Outline platelets.
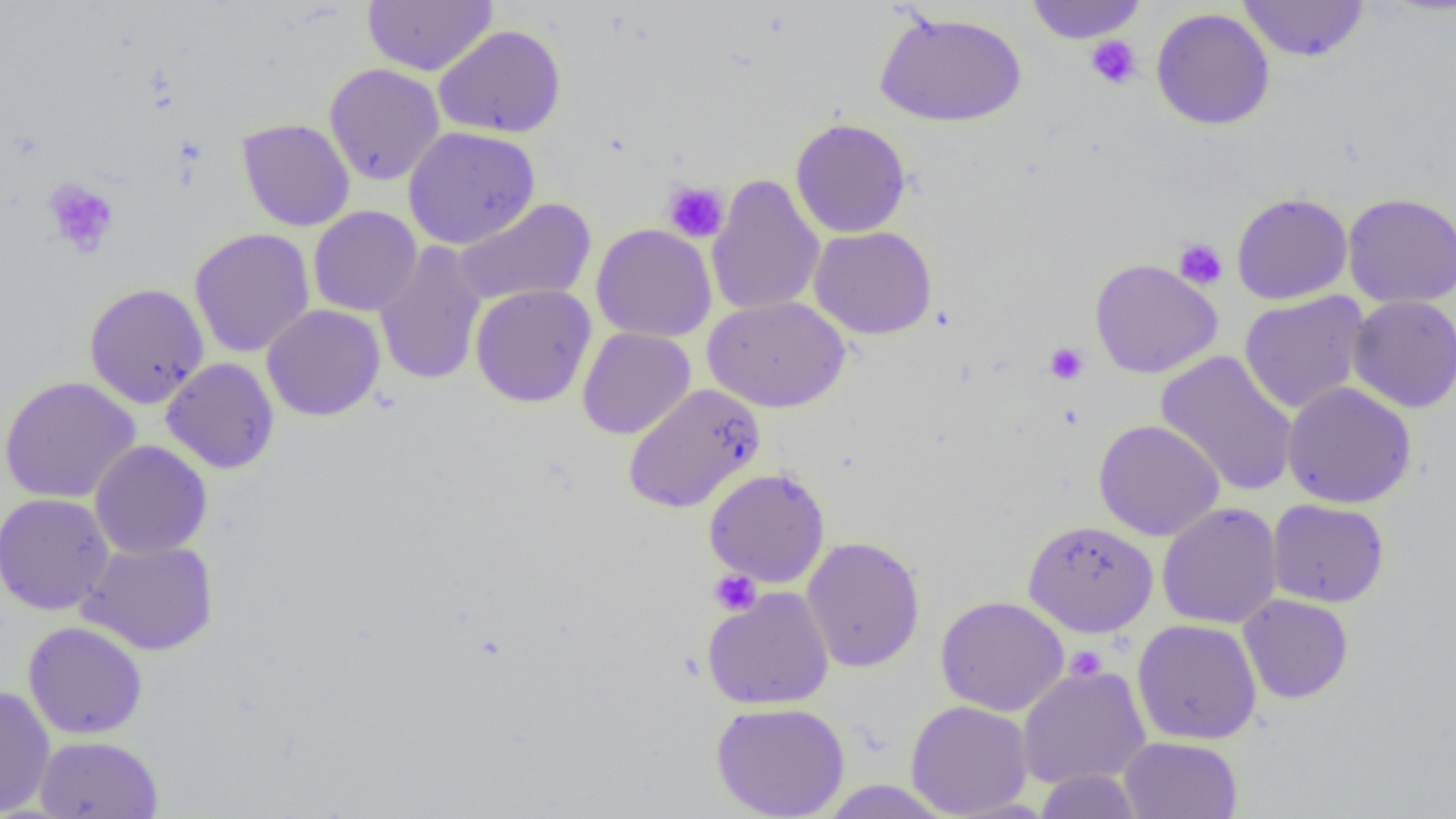

Approximate bounding boxes as [x1, y1, x2, y2] in pixels.
Platelets: [1085, 36, 1142, 89], [43, 178, 120, 258], [662, 180, 729, 243], [1174, 239, 1227, 290], [1044, 342, 1089, 385], [709, 570, 761, 616], [1066, 645, 1107, 682].

Summary:
  - Uninfected red blood cell locations: [362, 0, 497, 77], [1025, 0, 1147, 44], [1237, 0, 1371, 63], [1150, 7, 1275, 131], [874, 9, 1027, 127], [433, 24, 566, 139], [324, 63, 445, 186], [789, 117, 912, 239], [235, 118, 355, 232], [403, 126, 540, 249], [707, 174, 825, 317], [1231, 192, 1353, 305], [1342, 192, 1456, 308], [453, 197, 597, 306], [308, 205, 422, 317], [591, 224, 717, 343], [809, 226, 938, 340], [189, 228, 315, 358], [373, 241, 487, 387], [1089, 258, 1223, 379], [84, 282, 210, 409], [470, 283, 597, 408], [1238, 291, 1371, 415], [703, 295, 850, 413], [1347, 295, 1456, 413], [261, 304, 386, 422], [577, 327, 696, 440], [1155, 351, 1298, 497], [161, 357, 280, 474], [0, 376, 141, 503], [1282, 381, 1417, 509], [622, 383, 765, 514], [1093, 419, 1224, 541], [89, 440, 213, 560], [703, 467, 831, 588], [0, 493, 115, 615], [1267, 499, 1389, 608], [1157, 502, 1283, 630], [1023, 519, 1158, 637], [801, 536, 925, 673], [77, 538, 219, 656], [701, 586, 835, 709], [1238, 593, 1354, 704], [935, 595, 1069, 716], [1132, 618, 1262, 745], [23, 621, 148, 739], [1016, 664, 1151, 790], [0, 685, 56, 817], [905, 700, 1033, 818], [711, 701, 850, 818], [35, 735, 164, 818], [1118, 736, 1243, 818], [1034, 769, 1144, 818], [818, 780, 955, 818]
  - Slide-level diagnosis: negative for blood parasites
  - Field of view: one of a larger specimen
  - Image size: 1456×819 pixels
  - Modality: light microscopy
  - Preparation: thin blood film
  - Magnification: 1000x